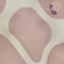 Malaria status: parasitized. Cell patch, automatically extracted from a larger field of view and resized to 64 × 64 pixels. Thin blood smear. Photographed with a smartphone camera at the microscope eyepiece. Giemsa stain.